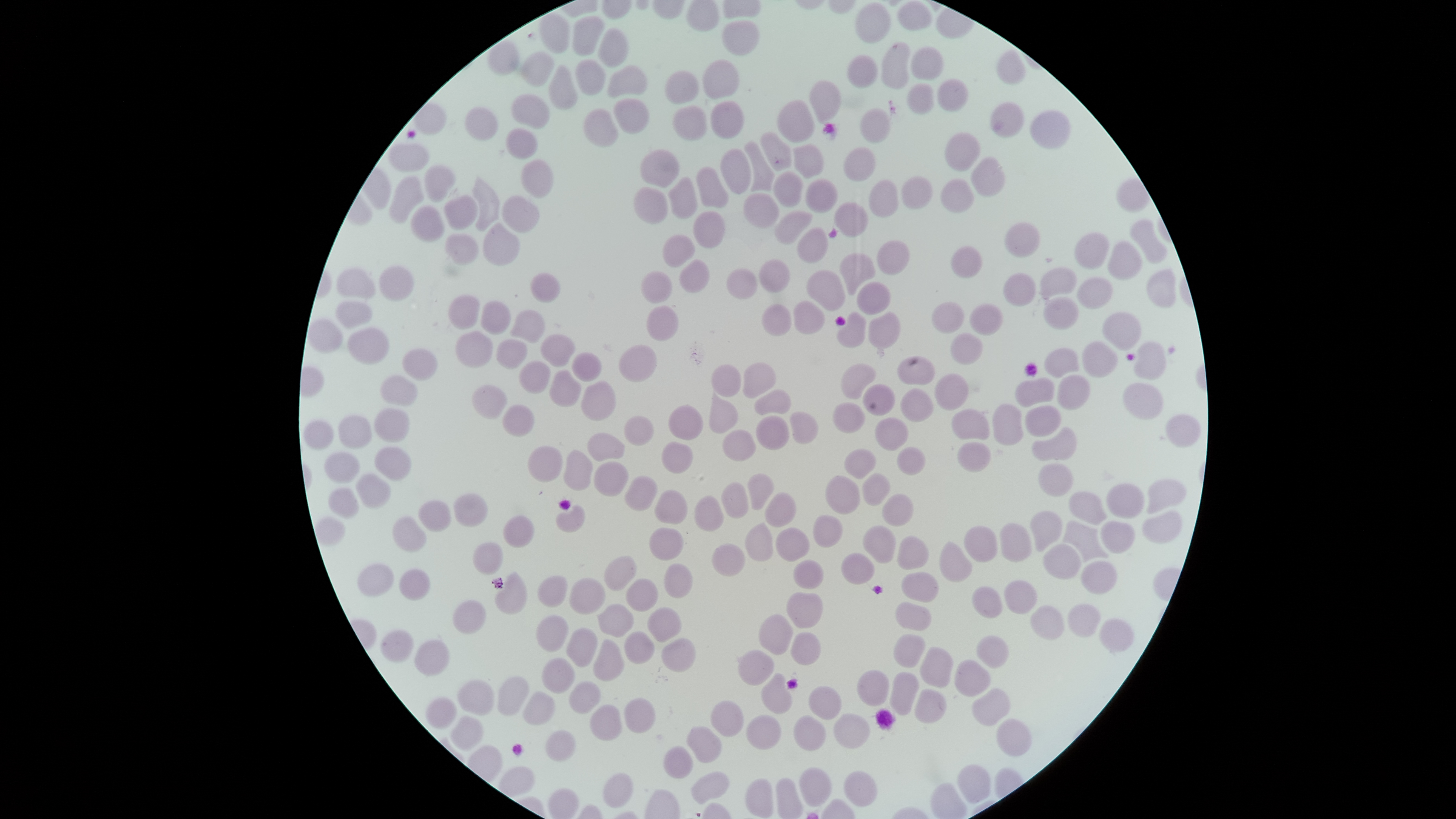

preparation = thin blood film
field of view = single
capture = smartphone photograph through the microscope eyepiece
stain = Giemsa
image size = 1456×819 pixels
uninfected red blood cells = approximate bounding boxes, in pixels from the top-left corner: (left=897, top=0, right=932, bottom=30), (left=855, top=1, right=891, bottom=43), (left=538, top=13, right=569, bottom=53), (left=572, top=15, right=605, bottom=56), (left=721, top=19, right=760, bottom=56), (left=598, top=28, right=630, bottom=68), (left=488, top=41, right=520, bottom=76), (left=880, top=41, right=910, bottom=89), (left=910, top=46, right=944, bottom=80), (left=996, top=50, right=1026, bottom=85), (left=520, top=51, right=554, bottom=87), (left=846, top=55, right=878, bottom=88), (left=575, top=59, right=606, bottom=96), (left=702, top=59, right=740, bottom=99), (left=607, top=64, right=648, bottom=98), (left=548, top=65, right=578, bottom=111), (left=664, top=70, right=699, bottom=105), (left=937, top=78, right=969, bottom=112), (left=808, top=79, right=841, bottom=122), (left=906, top=83, right=935, bottom=115), (left=510, top=93, right=550, bottom=129), (left=613, top=98, right=649, bottom=134), (left=710, top=100, right=745, bottom=138), (left=777, top=100, right=815, bottom=143), (left=990, top=101, right=1024, bottom=138), (left=414, top=103, right=447, bottom=135), (left=672, top=105, right=708, bottom=142), (left=465, top=106, right=499, bottom=141), (left=859, top=107, right=890, bottom=144), (left=582, top=109, right=619, bottom=147), (left=1029, top=110, right=1071, bottom=149), (left=505, top=128, right=539, bottom=160), (left=944, top=131, right=982, bottom=172), (left=760, top=132, right=792, bottom=171), (left=744, top=141, right=775, bottom=192), (left=388, top=142, right=430, bottom=172), (left=793, top=144, right=824, bottom=179), (left=843, top=146, right=876, bottom=182), (left=639, top=148, right=680, bottom=188), (left=720, top=148, right=752, bottom=194), (left=971, top=156, right=1006, bottom=197), (left=520, top=159, right=554, bottom=198), (left=424, top=164, right=456, bottom=202), (left=696, top=166, right=729, bottom=207), (left=773, top=171, right=804, bottom=206), (left=389, top=175, right=424, bottom=224), (left=472, top=176, right=499, bottom=231), (left=902, top=176, right=933, bottom=209), (left=668, top=177, right=698, bottom=219), (left=805, top=178, right=839, bottom=213), (left=939, top=178, right=975, bottom=213), (left=869, top=179, right=899, bottom=217), (left=633, top=187, right=668, bottom=225), (left=743, top=192, right=780, bottom=229), (left=443, top=194, right=478, bottom=230), (left=501, top=194, right=540, bottom=233), (left=834, top=202, right=869, bottom=238), (left=410, top=204, right=445, bottom=243), (left=693, top=210, right=726, bottom=248), (left=774, top=210, right=812, bottom=244), (left=1129, top=218, right=1167, bottom=264), (left=1004, top=222, right=1041, bottom=257), (left=483, top=223, right=520, bottom=266), (left=797, top=227, right=828, bottom=263), (left=1074, top=231, right=1110, bottom=270), (left=445, top=233, right=479, bottom=265), (left=662, top=233, right=696, bottom=268), (left=877, top=240, right=910, bottom=275), (left=1107, top=240, right=1143, bottom=280), (left=950, top=245, right=982, bottom=278), (left=839, top=252, right=876, bottom=296), (left=679, top=259, right=710, bottom=293), (left=759, top=259, right=790, bottom=293), (left=379, top=265, right=415, bottom=301), (left=1040, top=267, right=1077, bottom=300), (left=336, top=268, right=376, bottom=298), (left=726, top=268, right=757, bottom=300), (left=1146, top=268, right=1177, bottom=308), (left=640, top=270, right=673, bottom=304), (left=806, top=270, right=846, bottom=311), (left=1002, top=272, right=1036, bottom=307), (left=530, top=273, right=561, bottom=302), (left=1077, top=276, right=1113, bottom=309), (left=857, top=281, right=891, bottom=315), (left=447, top=294, right=480, bottom=329), (left=1043, top=296, right=1079, bottom=331), (left=336, top=300, right=373, bottom=329), (left=480, top=300, right=511, bottom=335), (left=793, top=301, right=825, bottom=334), (left=931, top=301, right=964, bottom=333), (left=761, top=303, right=792, bottom=336), (left=969, top=303, right=1002, bottom=336), (left=646, top=305, right=679, bottom=341), (left=510, top=309, right=546, bottom=343), (left=1103, top=310, right=1142, bottom=352), (left=868, top=311, right=901, bottom=350), (left=837, top=312, right=866, bottom=349), (left=307, top=317, right=343, bottom=353), (left=347, top=327, right=390, bottom=365), (left=454, top=330, right=493, bottom=368), (left=950, top=332, right=983, bottom=365), (left=540, top=333, right=576, bottom=367), (left=495, top=339, right=528, bottom=370), (left=1081, top=341, right=1118, bottom=378), (left=1133, top=341, right=1167, bottom=380), (left=618, top=344, right=657, bottom=382), (left=1044, top=347, right=1079, bottom=379), (left=402, top=348, right=438, bottom=380), (left=572, top=352, right=602, bottom=382), (left=897, top=355, right=936, bottom=385), (left=518, top=361, right=551, bottom=394), (left=742, top=361, right=776, bottom=398), (left=841, top=363, right=876, bottom=399), (left=711, top=364, right=741, bottom=397), (left=549, top=369, right=582, bottom=407), (left=934, top=373, right=970, bottom=411), (left=380, top=374, right=418, bottom=407), (left=1057, top=374, right=1091, bottom=410), (left=1014, top=377, right=1055, bottom=408), (left=581, top=381, right=616, bottom=421), (left=1123, top=382, right=1164, bottom=421), (left=471, top=384, right=508, bottom=419), (left=863, top=384, right=896, bottom=416), (left=900, top=388, right=934, bottom=422), (left=753, top=389, right=792, bottom=415), (left=709, top=393, right=738, bottom=433), (left=832, top=401, right=865, bottom=432), (left=503, top=404, right=534, bottom=437), (left=667, top=404, right=703, bottom=440), (left=992, top=404, right=1024, bottom=445), (left=1025, top=405, right=1062, bottom=437), (left=374, top=408, right=410, bottom=443), (left=951, top=408, right=990, bottom=440), (left=789, top=411, right=819, bottom=444), (left=338, top=414, right=372, bottom=449), (left=1165, top=414, right=1202, bottom=448), (left=624, top=415, right=654, bottom=446), (left=755, top=415, right=790, bottom=450), (left=874, top=417, right=909, bottom=451), (left=303, top=419, right=334, bottom=451), (left=1032, top=426, right=1077, bottom=462), (left=722, top=429, right=756, bottom=461), (left=586, top=432, right=625, bottom=461), (left=661, top=441, right=693, bottom=473), (left=957, top=441, right=992, bottom=473), (left=374, top=445, right=412, bottom=481), (left=527, top=445, right=562, bottom=483), (left=896, top=447, right=926, bottom=476), (left=844, top=448, right=877, bottom=479), (left=563, top=449, right=593, bottom=491), (left=323, top=451, right=360, bottom=484), (left=593, top=461, right=629, bottom=496), (left=1038, top=463, right=1074, bottom=497), (left=355, top=472, right=391, bottom=509), (left=747, top=473, right=774, bottom=510), (left=862, top=473, right=891, bottom=505), (left=624, top=475, right=658, bottom=511), (left=825, top=475, right=860, bottom=514), (left=1147, top=480, right=1186, bottom=514), (left=721, top=482, right=749, bottom=518), (left=1106, top=485, right=1145, bottom=519), (left=327, top=487, right=359, bottom=517), (left=654, top=489, right=688, bottom=525), (left=1068, top=491, right=1106, bottom=525), (left=453, top=492, right=488, bottom=527), (left=764, top=492, right=797, bottom=527), (left=882, top=493, right=914, bottom=526), (left=694, top=495, right=724, bottom=531), (left=418, top=500, right=451, bottom=532), (left=556, top=504, right=585, bottom=533), (left=1029, top=510, right=1063, bottom=552), (left=1142, top=512, right=1182, bottom=544), (left=502, top=515, right=535, bottom=548), (left=812, top=515, right=843, bottom=548), (left=392, top=516, right=427, bottom=553), (left=315, top=517, right=346, bottom=546), (left=1062, top=521, right=1110, bottom=563), (left=1101, top=521, right=1134, bottom=554), (left=744, top=522, right=774, bottom=561), (left=999, top=522, right=1032, bottom=562), (left=862, top=525, right=896, bottom=564), (left=964, top=526, right=998, bottom=562), (left=648, top=527, right=683, bottom=561), (left=776, top=527, right=810, bottom=562), (left=897, top=535, right=929, bottom=570), (left=939, top=541, right=973, bottom=582), (left=472, top=542, right=504, bottom=575), (left=711, top=543, right=745, bottom=577), (left=1043, top=544, right=1081, bottom=580), (left=840, top=553, right=875, bottom=585), (left=604, top=555, right=637, bottom=591), (left=793, top=559, right=824, bottom=589), (left=1080, top=561, right=1117, bottom=594), (left=357, top=563, right=394, bottom=598), (left=663, top=563, right=693, bottom=599), (left=399, top=568, right=430, bottom=601), (left=494, top=571, right=528, bottom=615), (left=901, top=571, right=939, bottom=603), (left=537, top=575, right=567, bottom=608), (left=569, top=577, right=606, bottom=615), (left=625, top=578, right=658, bottom=612), (left=1004, top=580, right=1038, bottom=615), (left=971, top=586, right=1003, bottom=618), (left=786, top=591, right=823, bottom=629), (left=452, top=599, right=486, bottom=634), (left=894, top=601, right=932, bottom=631), (left=597, top=603, right=634, bottom=638), (left=1068, top=604, right=1100, bottom=637), (left=1030, top=605, right=1065, bottom=640), (left=647, top=606, right=683, bottom=643), (left=536, top=614, right=569, bottom=653), (left=758, top=614, right=794, bottom=655), (left=1100, top=620, right=1133, bottom=652), (left=566, top=627, right=598, bottom=668), (left=380, top=629, right=414, bottom=662), (left=624, top=630, right=655, bottom=665), (left=790, top=631, right=821, bottom=665), (left=893, top=633, right=926, bottom=668), (left=976, top=635, right=1009, bottom=668), (left=661, top=637, right=697, bottom=673), (left=415, top=639, right=450, bottom=675), (left=593, top=639, right=625, bottom=681), (left=919, top=646, right=954, bottom=688), (left=738, top=649, right=775, bottom=686), (left=541, top=658, right=575, bottom=694), (left=954, top=659, right=991, bottom=696), (left=856, top=669, right=890, bottom=706), (left=890, top=671, right=920, bottom=716), (left=761, top=673, right=794, bottom=714), (left=497, top=676, right=529, bottom=716), (left=457, top=679, right=494, bottom=716), (left=568, top=680, right=601, bottom=714), (left=808, top=685, right=842, bottom=720), (left=972, top=687, right=1011, bottom=726), (left=914, top=689, right=947, bottom=724), (left=522, top=690, right=556, bottom=726), (left=425, top=697, right=457, bottom=729), (left=624, top=697, right=656, bottom=733), (left=710, top=700, right=744, bottom=737), (left=589, top=704, right=622, bottom=740), (left=833, top=712, right=871, bottom=749), (left=746, top=714, right=782, bottom=750), (left=793, top=714, right=826, bottom=751), (left=450, top=716, right=483, bottom=751), (left=996, top=718, right=1032, bottom=756), (left=686, top=725, right=722, bottom=763), (left=545, top=729, right=576, bottom=762), (left=663, top=745, right=693, bottom=779), (left=958, top=764, right=991, bottom=804), (left=799, top=767, right=832, bottom=807), (left=843, top=769, right=878, bottom=806), (left=690, top=771, right=730, bottom=805), (left=602, top=772, right=634, bottom=809), (left=744, top=778, right=774, bottom=818)
presence = no malaria parasites identified
visible region = circular